Point out each Plasmodium parasite.
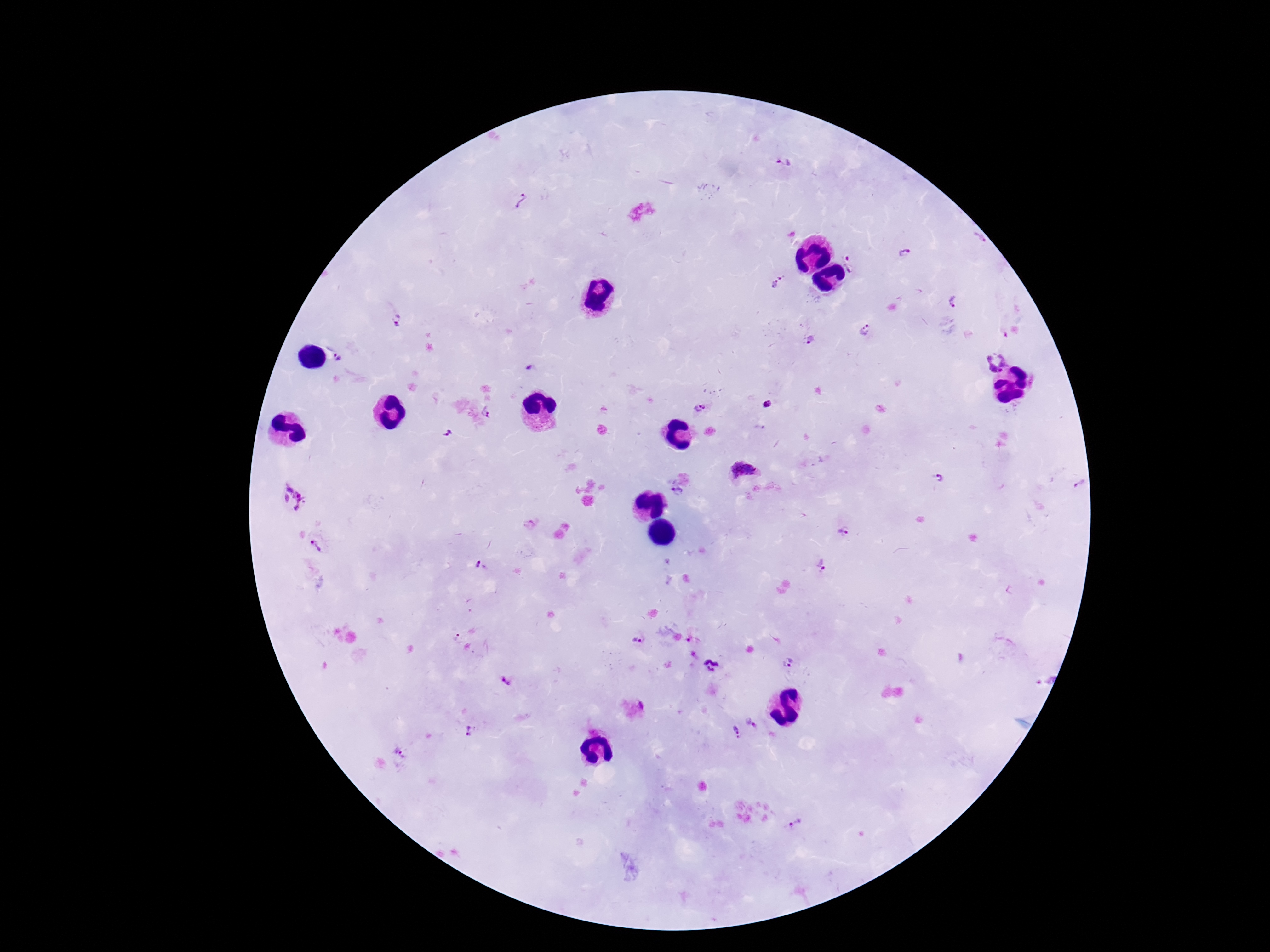
Approximate centers as {x, y} in pixels.
Plasmodium parasites: {783, 161}, {522, 201}, {904, 253}, {852, 263}, {781, 275}, {775, 285}, {955, 301}, {398, 319}, {867, 331}, {812, 341}, {338, 358}, {995, 360}, {530, 367}, {768, 404}, {699, 408}, {487, 411}, {448, 434}, {745, 470}, {941, 479}, {1081, 483}, {677, 494}, {291, 499}, {843, 532}, {315, 545}, {478, 564}, {822, 566}, {455, 636}, {637, 643}, {787, 661}, {712, 664}, {505, 682}, {753, 721}, {469, 730}, {736, 732}, {405, 756}, {798, 824}.

Summary:
  - Image size: 1270×952 pixels
  - Magnification: 100x
  - Preparation: thick blood film
  - Field of view: one from this slide
  - Capture: smartphone camera through the microscope eyepiece
  - Stain: Giemsa
  - Patient malaria status: infected